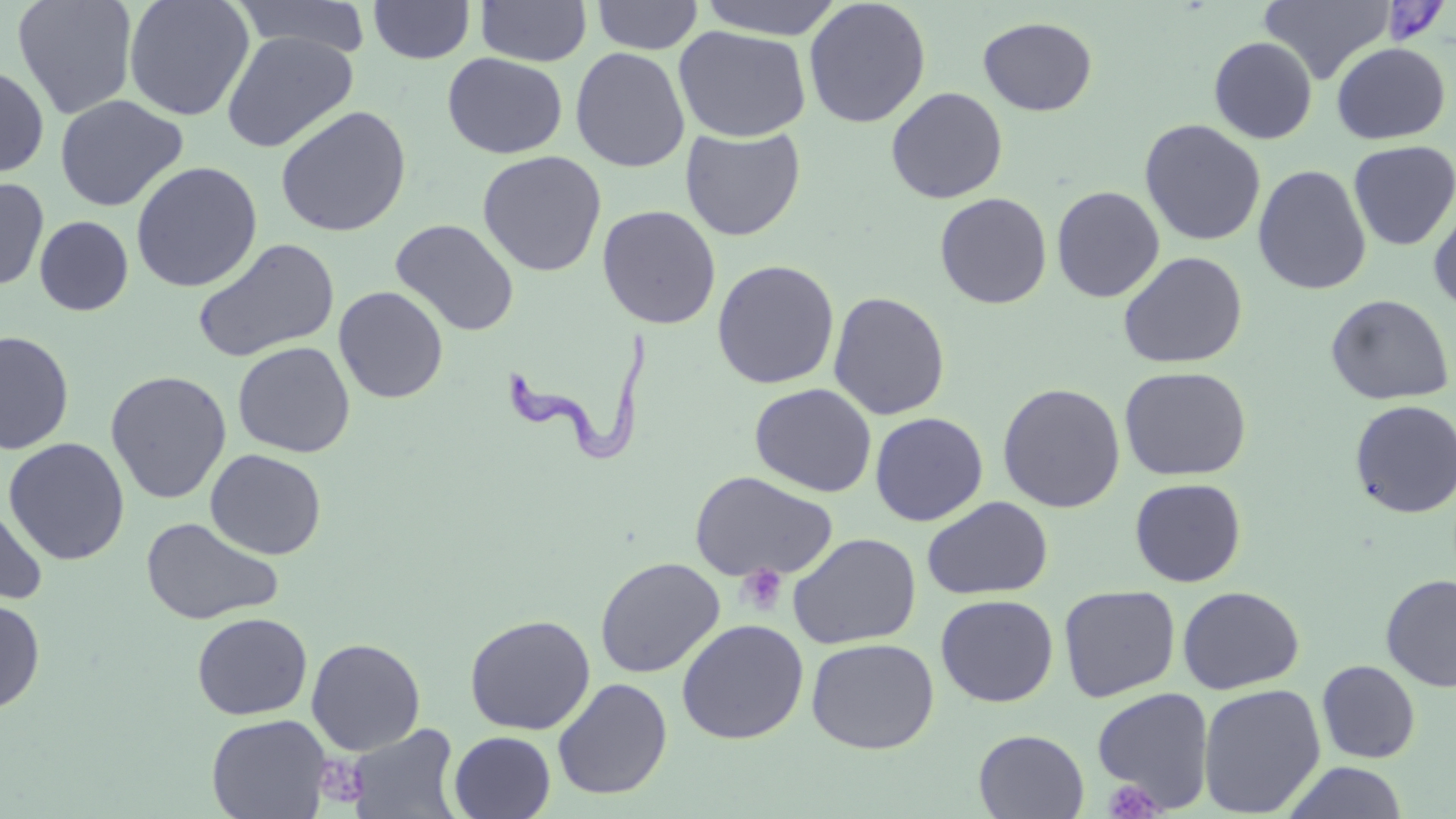

slide-level diagnosis = Trypanosoma brucei
platelet locations = approximate bounding boxes as (x1,y1)-(x2,y2) corner pairs in pixels: (736,565)-(788,616), (315,754)-(370,808), (1103,779)-(1163,819)
field of view = single
Trypanosoma brucei locations = approximate bounding boxes as (x1,y1)-(x2,y2) corner pairs in pixels: (503,333)-(658,467)
image size = 1456×819 pixels
magnification = 1000x
uninfected red blood cell locations = approximate bounding boxes as (x1,y1)-(x2,y2) corner pairs in pixels: (12,0)-(139,119), (124,0)-(254,121), (230,0)-(373,59), (591,0)-(704,54), (696,0)-(848,40), (1258,0)-(1396,85), (368,1)-(476,64), (476,1)-(592,67), (803,1)-(931,129), (978,16)-(1097,117), (673,26)-(811,142), (220,30)-(358,153), (1208,36)-(1318,144), (1330,41)-(1451,145), (570,47)-(690,172), (442,53)-(567,159), (0,64)-(50,179), (886,87)-(1008,204), (54,94)-(188,212), (275,106)-(412,237), (1140,119)-(1266,246), (680,126)-(807,241), (1348,140)-(1455,250), (477,150)-(607,277), (131,161)-(263,292), (1252,164)-(1372,295), (0,175)-(49,291), (1051,185)-(1165,302), (934,192)-(1053,309), (1428,201)-(1456,315), (597,205)-(721,330), (34,215)-(134,316), (390,218)-(520,337), (192,238)-(340,363), (1117,251)-(1248,369), (712,259)-(840,389), (333,286)-(448,404), (828,291)-(950,421), (1325,294)-(1453,406), (0,331)-(75,455), (232,341)-(355,458), (1119,365)-(1252,481), (105,370)-(232,504), (997,382)-(1126,513), (750,383)-(877,497), (1349,399)-(1456,518), (870,412)-(988,526), (3,438)-(130,565), (205,449)-(327,560), (689,471)-(838,582), (1129,478)-(1246,587), (922,496)-(1053,600), (0,497)-(48,608), (141,516)-(284,626), (787,532)-(922,650), (594,557)-(725,678), (1380,573)-(1456,692), (1058,585)-(1181,702), (1177,585)-(1305,694), (935,594)-(1059,707), (0,597)-(45,713), (191,612)-(312,720), (464,614)-(596,735), (676,619)-(809,744), (306,637)-(426,756), (805,637)-(940,754), (1317,660)-(1421,764), (552,678)-(672,800), (1198,683)-(1326,817), (1091,687)-(1215,812), (206,714)-(331,819), (346,724)-(463,819), (973,729)-(1089,818), (449,731)-(556,818), (1282,762)-(1410,819)
preparation = thin blood smear
modality = optical microscopy
stain = May-Grünwald-Giemsa